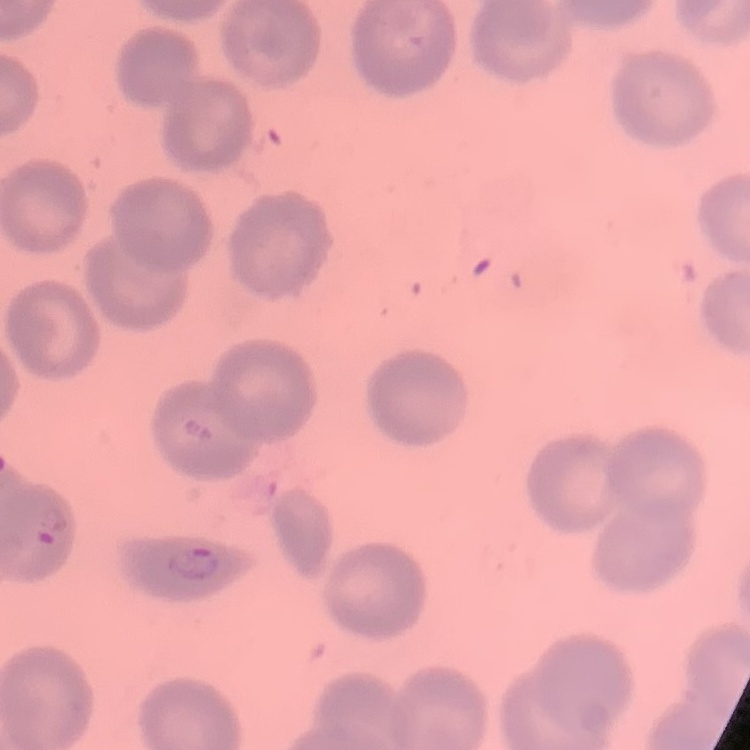

The red blood cells show no rouleaux formation. One tile cut from a larger photomicrograph. Thin blood smear. Stained with either Field's or Giemsa.